Locate and identify every blood parasite.
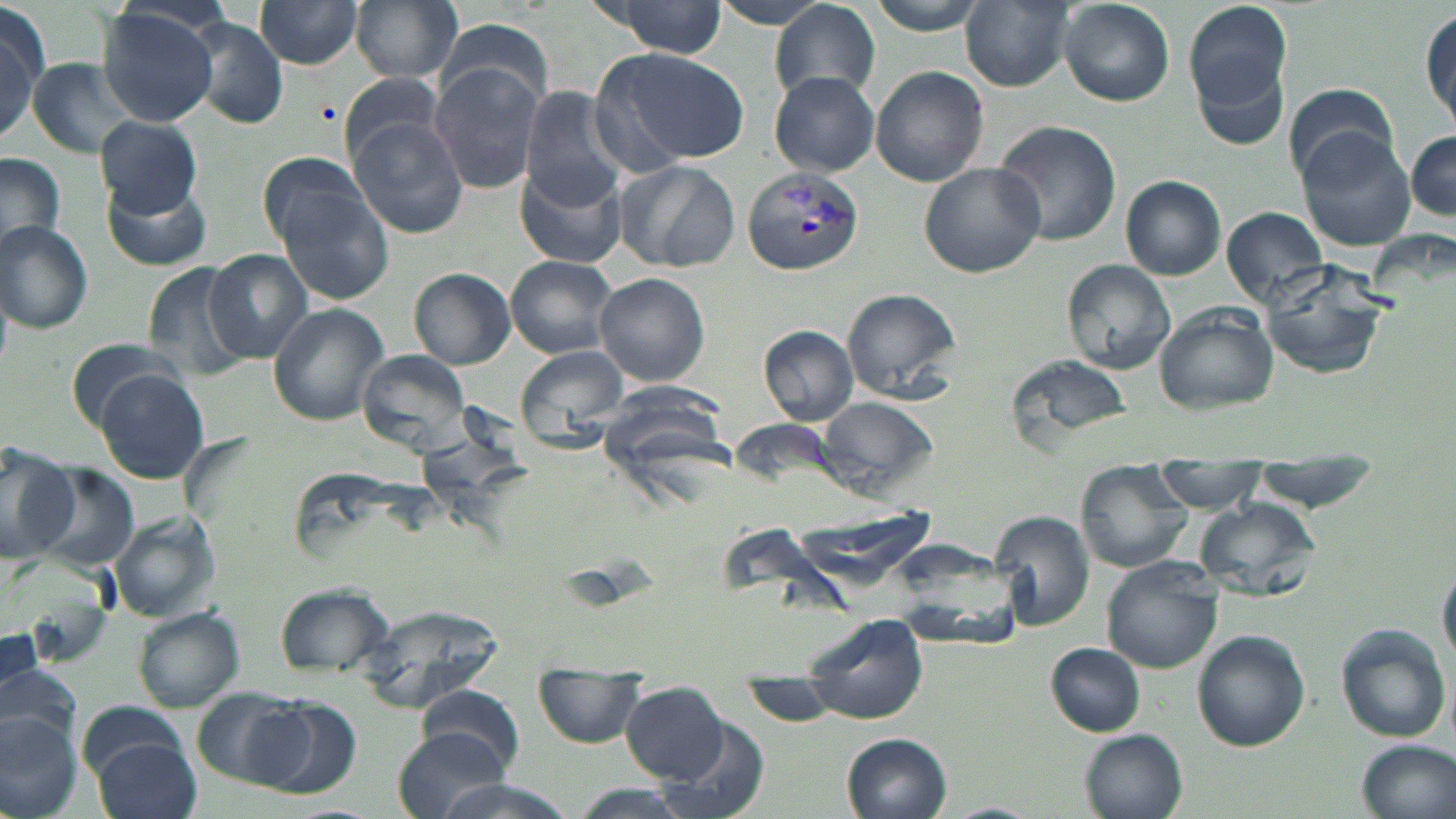

Approximate bounding boxes as named x1/y1/x2/y2 corners in pixels.
Plasmodium vivax-infected red blood cells: (x1=743, y1=167, x2=867, y2=275).
No Plasmodium falciparum, Plasmodium ovale, Plasmodium malariae, Babesia divergens, or Trypanosoma brucei observed.

Uninfected red blood cell locations: (x1=350, y1=0, x2=463, y2=83), (x1=866, y1=0, x2=990, y2=35), (x1=1185, y1=0, x2=1295, y2=121), (x1=252, y1=1, x2=364, y2=70), (x1=961, y1=1, x2=1076, y2=90), (x1=594, y1=2, x2=731, y2=56), (x1=708, y1=2, x2=840, y2=30), (x1=1060, y1=2, x2=1174, y2=106), (x1=771, y1=3, x2=881, y2=104), (x1=96, y1=6, x2=223, y2=126), (x1=0, y1=7, x2=46, y2=144), (x1=1420, y1=10, x2=1454, y2=131), (x1=186, y1=18, x2=291, y2=130), (x1=436, y1=19, x2=555, y2=117), (x1=599, y1=46, x2=748, y2=164), (x1=26, y1=59, x2=141, y2=159), (x1=1193, y1=59, x2=1290, y2=151), (x1=429, y1=60, x2=547, y2=193), (x1=871, y1=66, x2=990, y2=186), (x1=770, y1=71, x2=881, y2=176), (x1=336, y1=73, x2=449, y2=164), (x1=1282, y1=83, x2=1403, y2=188), (x1=518, y1=86, x2=627, y2=205), (x1=96, y1=116, x2=206, y2=215), (x1=993, y1=120, x2=1122, y2=246), (x1=350, y1=121, x2=470, y2=238), (x1=1296, y1=128, x2=1417, y2=251), (x1=1405, y1=131, x2=1456, y2=224), (x1=260, y1=151, x2=368, y2=247), (x1=0, y1=154, x2=66, y2=255), (x1=614, y1=158, x2=739, y2=270), (x1=920, y1=161, x2=1044, y2=278), (x1=515, y1=162, x2=625, y2=270), (x1=273, y1=175, x2=397, y2=307), (x1=1121, y1=175, x2=1226, y2=279), (x1=100, y1=181, x2=214, y2=271), (x1=1223, y1=207, x2=1328, y2=306), (x1=0, y1=221, x2=95, y2=333), (x1=205, y1=248, x2=314, y2=361), (x1=505, y1=256, x2=619, y2=358), (x1=1061, y1=259, x2=1176, y2=372), (x1=142, y1=260, x2=255, y2=380), (x1=1262, y1=265, x2=1391, y2=378), (x1=409, y1=268, x2=515, y2=368), (x1=593, y1=273, x2=710, y2=385), (x1=841, y1=287, x2=962, y2=401), (x1=267, y1=304, x2=388, y2=426), (x1=1154, y1=305, x2=1277, y2=414), (x1=758, y1=324, x2=860, y2=426), (x1=63, y1=337, x2=192, y2=435), (x1=516, y1=346, x2=626, y2=432), (x1=356, y1=348, x2=471, y2=454), (x1=1005, y1=350, x2=1135, y2=451), (x1=96, y1=368, x2=209, y2=485), (x1=815, y1=395, x2=939, y2=501), (x1=0, y1=441, x2=78, y2=565), (x1=1153, y1=461, x2=1266, y2=512), (x1=1075, y1=462, x2=1190, y2=573), (x1=1250, y1=462, x2=1381, y2=508), (x1=34, y1=466, x2=142, y2=574), (x1=1196, y1=498, x2=1321, y2=600), (x1=113, y1=511, x2=223, y2=621), (x1=992, y1=513, x2=1096, y2=632), (x1=1101, y1=559, x2=1221, y2=673), (x1=1438, y1=561, x2=1456, y2=668), (x1=271, y1=582, x2=394, y2=683), (x1=356, y1=601, x2=502, y2=712), (x1=132, y1=607, x2=244, y2=712), (x1=1335, y1=624, x2=1453, y2=743), (x1=0, y1=629, x2=46, y2=713), (x1=1192, y1=631, x2=1311, y2=752), (x1=806, y1=634, x2=931, y2=719), (x1=1045, y1=643, x2=1146, y2=737), (x1=2, y1=664, x2=82, y2=751), (x1=535, y1=665, x2=643, y2=747), (x1=417, y1=685, x2=525, y2=775), (x1=621, y1=685, x2=732, y2=783), (x1=192, y1=689, x2=305, y2=786), (x1=254, y1=698, x2=363, y2=796), (x1=79, y1=700, x2=192, y2=783), (x1=0, y1=714, x2=81, y2=819), (x1=654, y1=720, x2=774, y2=819), (x1=391, y1=727, x2=511, y2=819), (x1=1080, y1=728, x2=1189, y2=819), (x1=841, y1=733, x2=954, y2=819), (x1=91, y1=736, x2=202, y2=819), (x1=1354, y1=739, x2=1456, y2=819), (x1=425, y1=777, x2=577, y2=819), (x1=563, y1=785, x2=701, y2=819), (x1=939, y1=802, x2=1042, y2=819). Slide-level diagnosis: Plasmodium vivax. May-Grünwald-Giemsa stain. Image is 1456×819 pixels. Light microscopy. One field of a larger specimen. Captured at 1000x magnification. Thin blood smear.